Report the malaria status of this cell.
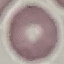

It is uninfected.

capture = smartphone through the microscope eyepiece
preparation = thin blood smear
stain = Giemsa
image type = automatically extracted cell patch, resized to 64 × 64 pixels